Outline each blood parasite and name the species.
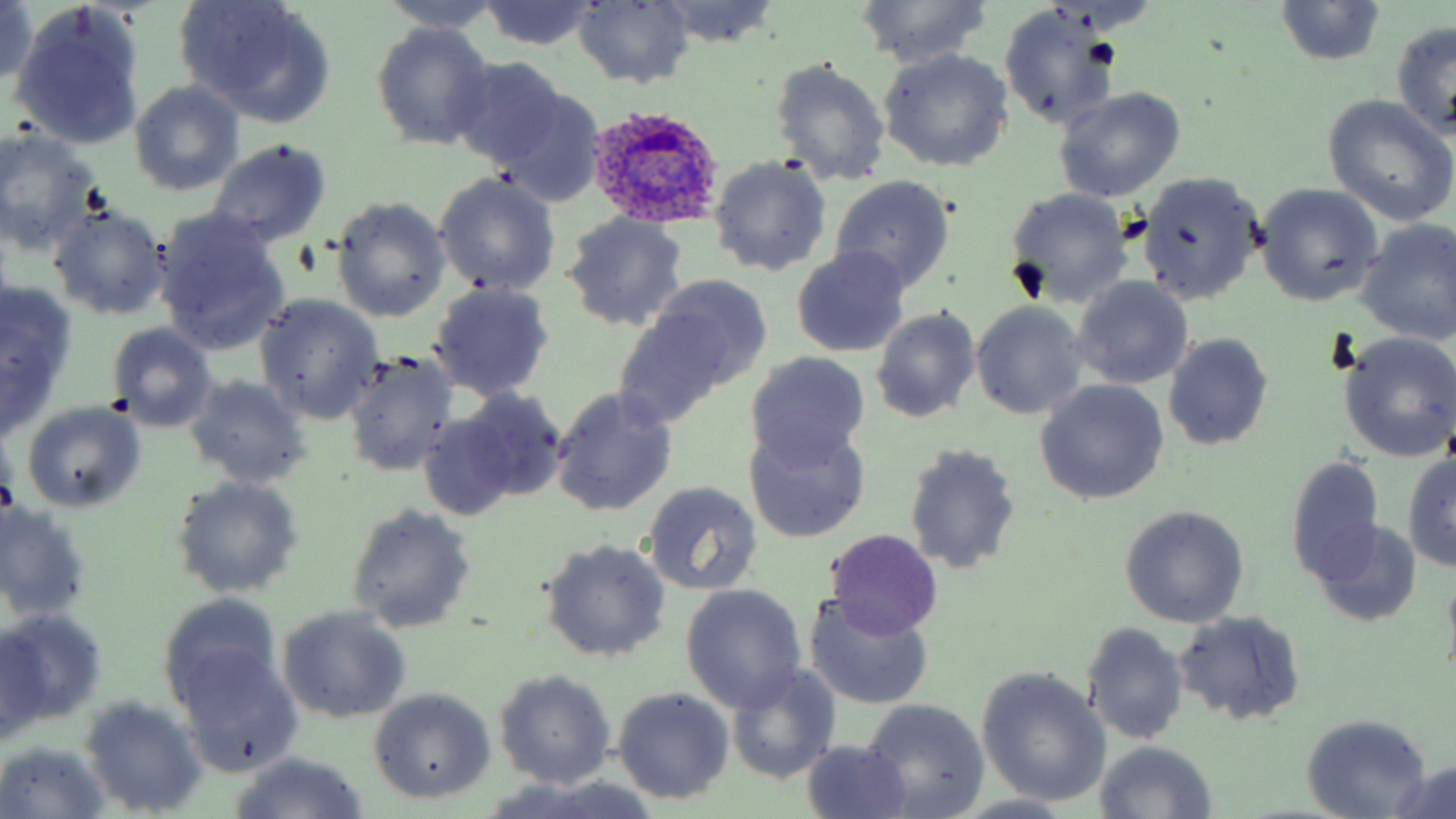

Approximate bounding boxes as [x1, y1, x2, y2] in pixels.
Plasmodium ovale-infected red blood cells: [586, 102, 725, 229].
No Plasmodium falciparum, Plasmodium malariae, Plasmodium vivax, Babesia divergens, or Trypanosoma brucei observed.

Uninfected red blood cell locations: [175, 0, 337, 128], [1275, 0, 1387, 69], [479, 1, 601, 50], [573, 1, 695, 87], [654, 1, 781, 47], [853, 1, 996, 69], [2, 2, 42, 87], [378, 2, 504, 34], [10, 5, 146, 150], [997, 5, 1122, 134], [370, 21, 497, 150], [1390, 21, 1456, 140], [878, 49, 1013, 172], [450, 56, 568, 173], [769, 56, 892, 187], [130, 83, 243, 195], [1054, 88, 1186, 203], [493, 89, 606, 207], [1323, 95, 1456, 227], [1, 129, 100, 257], [206, 138, 334, 247], [708, 155, 832, 278], [433, 171, 561, 298], [1137, 172, 1265, 304], [830, 175, 955, 296], [1257, 184, 1384, 306], [1003, 187, 1134, 309], [331, 198, 451, 323], [46, 202, 169, 322], [151, 207, 288, 354], [560, 213, 691, 332], [1355, 219, 1456, 346], [792, 248, 912, 358], [647, 273, 773, 393], [1071, 275, 1193, 390], [428, 282, 556, 403], [1, 283, 76, 404], [254, 295, 384, 425], [969, 302, 1089, 420], [613, 305, 740, 426], [870, 307, 981, 423], [105, 322, 219, 432], [1163, 333, 1274, 452], [1338, 333, 1456, 463], [341, 351, 460, 476], [743, 351, 870, 468], [185, 375, 313, 490], [1033, 380, 1169, 505], [459, 386, 568, 502], [551, 386, 678, 517], [20, 400, 146, 511], [418, 413, 516, 521], [743, 420, 870, 543], [902, 443, 1022, 575], [1287, 455, 1387, 585], [1402, 455, 1456, 573], [171, 476, 305, 598], [641, 481, 763, 596], [346, 503, 478, 634], [0, 504, 93, 623], [1120, 504, 1249, 627], [1311, 521, 1419, 625], [824, 529, 943, 639], [539, 539, 671, 662], [680, 585, 807, 711], [159, 590, 283, 711], [803, 592, 935, 711], [277, 606, 412, 725], [0, 609, 106, 724], [1174, 611, 1306, 726], [1081, 623, 1190, 745], [1, 633, 51, 745], [177, 651, 301, 777], [727, 665, 839, 783], [976, 668, 1111, 806], [494, 670, 615, 790], [613, 687, 734, 803], [369, 688, 496, 803], [78, 695, 209, 816], [862, 699, 990, 818], [1300, 715, 1431, 818], [801, 739, 913, 818], [0, 741, 111, 817], [1094, 742, 1216, 818], [225, 752, 371, 819], [1388, 763, 1456, 816], [484, 781, 662, 819], [950, 795, 1082, 819]. Slide-level diagnosis: Plasmodium ovale. One field of a larger specimen. Captured at 1000x magnification. May-Grünwald-Giemsa-stained preparation. Image is 1456×819 pixels. Thin blood film. Light microscopy.